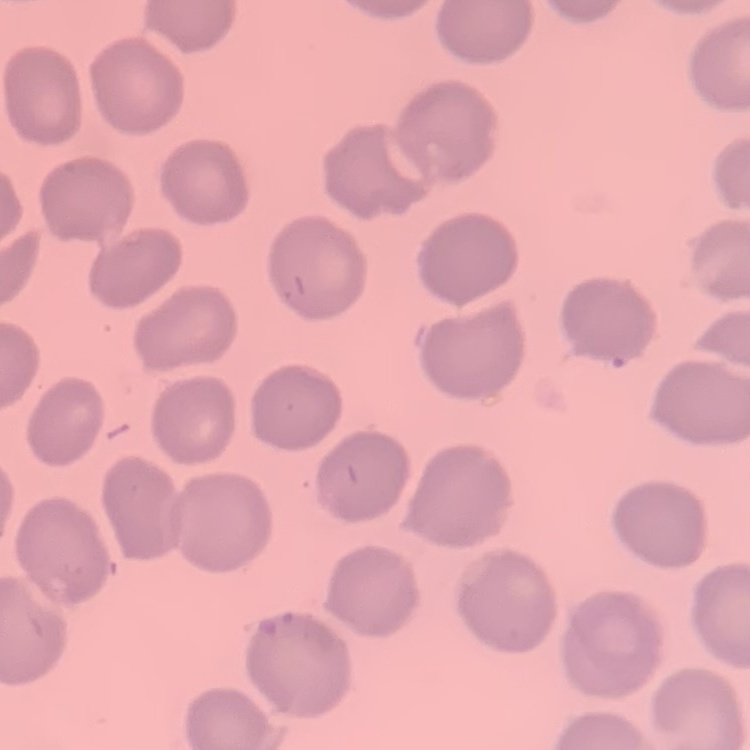

Summary:
  - Erythrocyte morphology: no rouleaux formation
  - Image type: one tile cut from a larger photomicrograph
  - Stain: Field's or Giemsa
  - Preparation: thin blood smear